Identify the parasite.
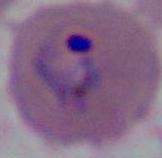

This is Plasmodium.

{
  "magnification": "400x or 1000x",
  "modality": "photomicrograph"
}